Report the malaria status of this cell.
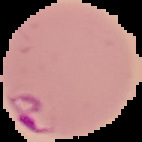
It is parasitized.

Summary:
  - Preparation: thin blood smear
  - Image type: segmented cell region on a black background
  - Image size: 142×142 pixels